Give the extent of all uninfected red blood cells.
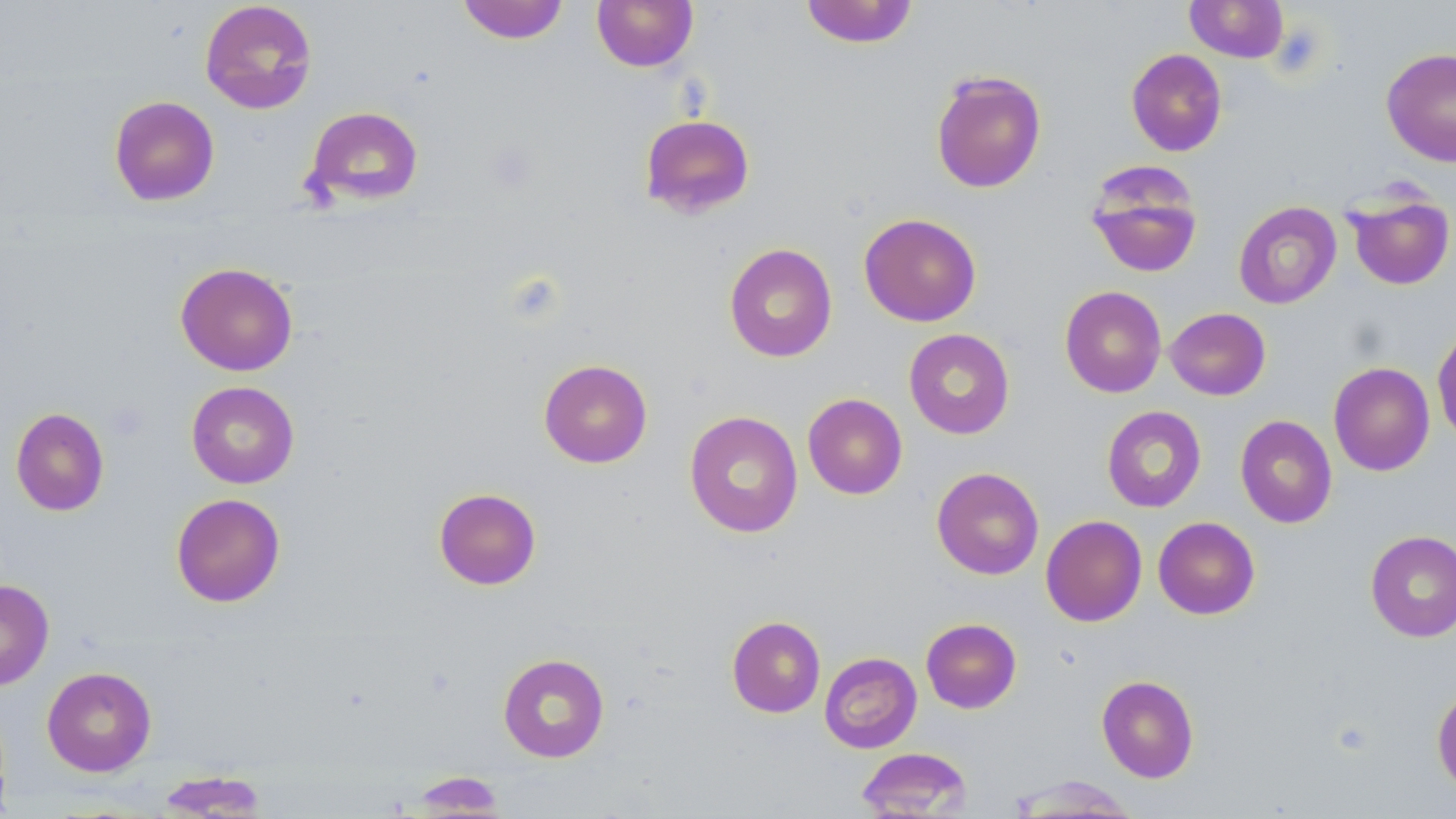

Approximate bounding boxes as [x1, y1, x2, y2] in pixels.
Uninfected red blood cells: [199, 0, 318, 115], [457, 0, 569, 44], [592, 0, 698, 72], [800, 0, 919, 48], [1185, 0, 1288, 62], [1381, 47, 1456, 167], [1125, 48, 1227, 157], [930, 69, 1047, 193], [109, 95, 220, 206], [303, 105, 424, 207], [639, 113, 756, 219], [1085, 164, 1204, 279], [1343, 188, 1455, 291], [1233, 201, 1342, 309], [859, 213, 981, 326], [724, 243, 838, 363], [175, 262, 299, 376], [1059, 285, 1167, 398], [1165, 307, 1271, 400], [1432, 326, 1456, 444], [903, 328, 1015, 439], [538, 359, 653, 468], [1328, 361, 1435, 476], [186, 381, 300, 489], [802, 393, 907, 499], [1101, 405, 1207, 513], [10, 407, 109, 516], [684, 410, 803, 538], [1235, 415, 1337, 528], [931, 466, 1044, 580], [433, 487, 541, 590], [170, 492, 286, 607], [1041, 515, 1147, 626], [1153, 516, 1260, 619], [1365, 530, 1456, 642], [0, 579, 54, 690], [727, 615, 825, 718], [921, 618, 1022, 713], [498, 652, 609, 762], [819, 652, 922, 753], [42, 666, 157, 777], [1096, 675, 1199, 782], [1432, 686, 1456, 794], [856, 747, 974, 818], [155, 771, 271, 817], [407, 772, 510, 816], [1007, 776, 1144, 817].

slide_level_diagnosis: negative for blood parasites
field_of_view: single
preparation: thin blood film
image_size: 1456×819 pixels
magnification: 1000x
modality: light microscopy
stain: May-Grünwald-Giemsa